Name the parasite shown.
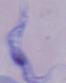

This is a trypanosome.

magnification = 1000x
modality = micrograph